Identify the parasite.
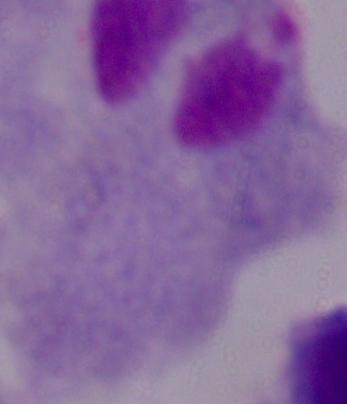

This is a trichomonad.

Micrograph. Captured at 1000x magnification.